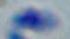
{
  "modality": "micrograph",
  "identification": "Toxoplasma gondii",
  "magnification": "1000x"
}